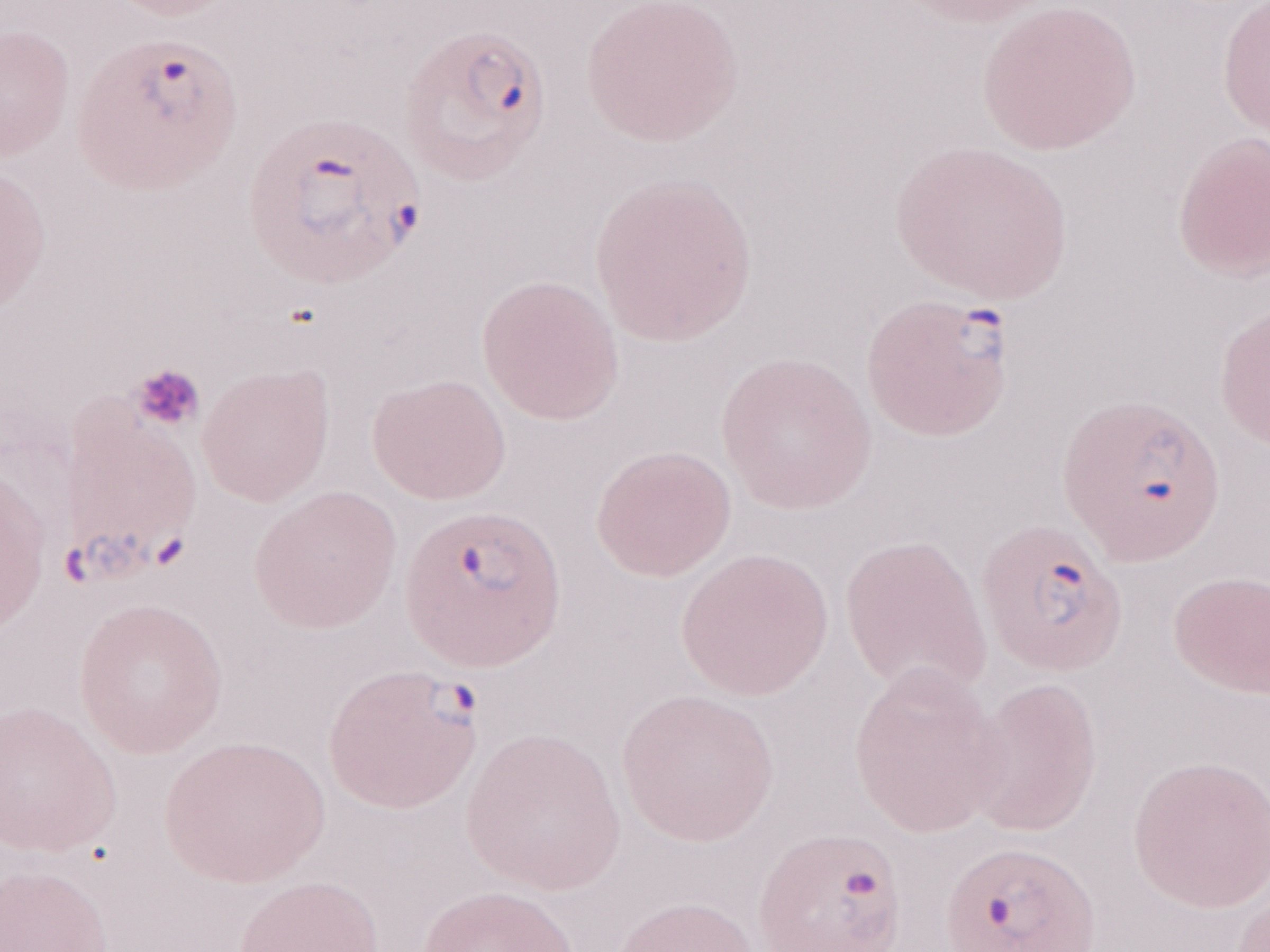 One field of this slide. Malaria diagnosis (patient-level): positive. Image is 1270×952 pixels. May-Grünwald-Giemsa (MGG) stain. 1,000x magnification. Olympus BX43 microscope and DP73 digital camera. Thin blood film.